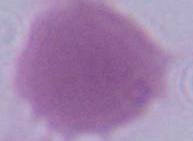
magnification = 1000x
identification = red blood cell
modality = micrograph